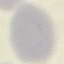
Summary:
  - Malaria status: uninfected
  - Capture: smartphone through the microscope eyepiece
  - Preparation: thin blood film
  - Image type: automatically extracted cell patch, resized to 64 × 64 pixels
  - Stain: Giemsa